Locate every Plasmodium parasite.
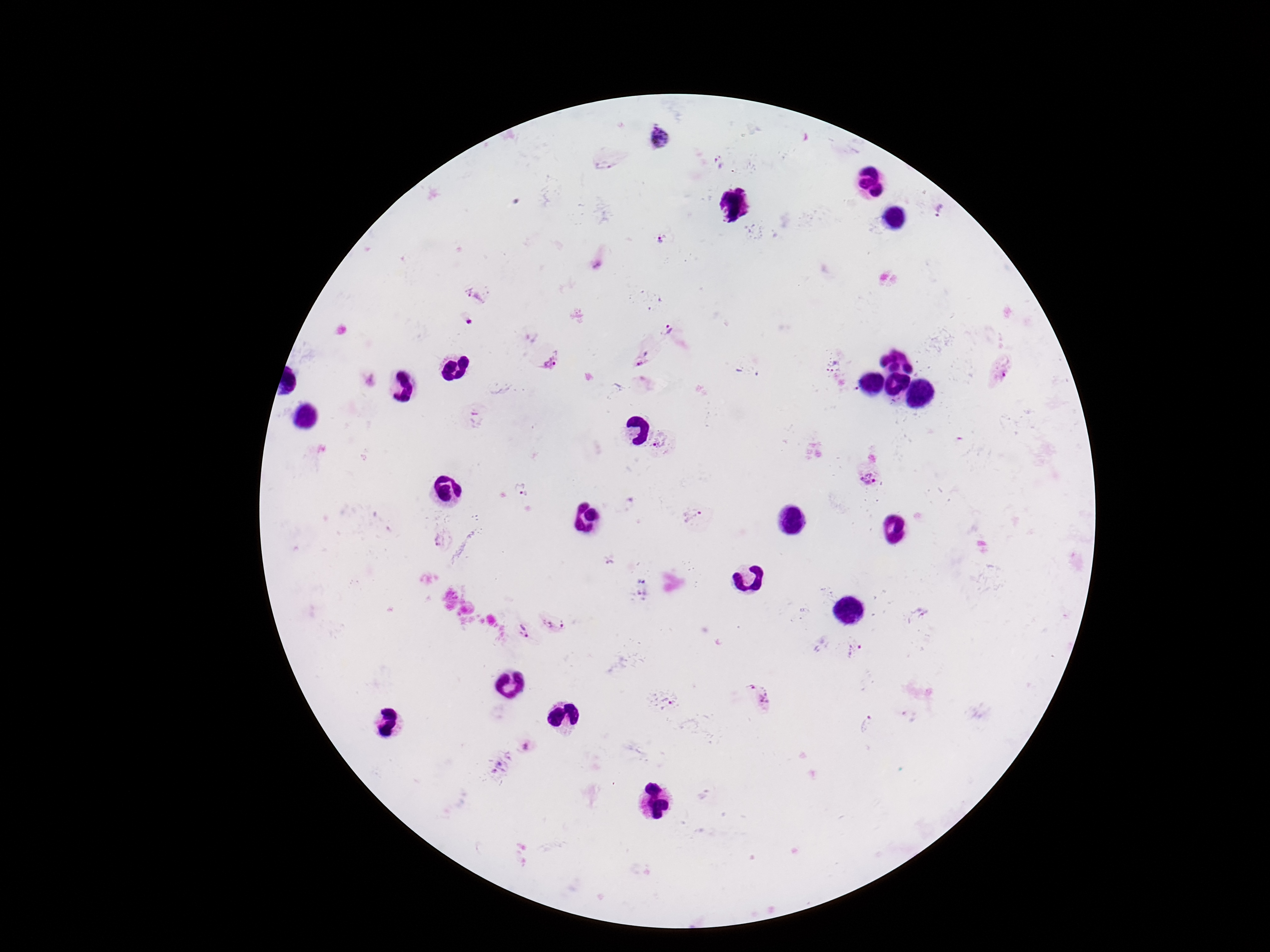
Approximate centers as {x, y} in pixels.
Plasmodium parasites: {660, 138}, {718, 164}, {603, 165}, {941, 211}, {661, 240}, {474, 294}, {469, 324}, {671, 331}, {641, 360}, {552, 362}, {1000, 371}, {662, 445}, {868, 477}, {524, 495}, {690, 517}, {441, 541}, {610, 564}, {917, 616}, {555, 624}, {525, 633}, {854, 650}, {750, 685}, {764, 699}, {673, 706}, {867, 723}, {525, 745}, {500, 765}.

capture = smartphone camera through the microscope eyepiece
patient malaria status = positive
stain = Giemsa
image size = 1270×952 pixels
preparation = thick blood smear
magnification = 100x
field of view = one from this slide